Assess the morphology of the red blood cells.
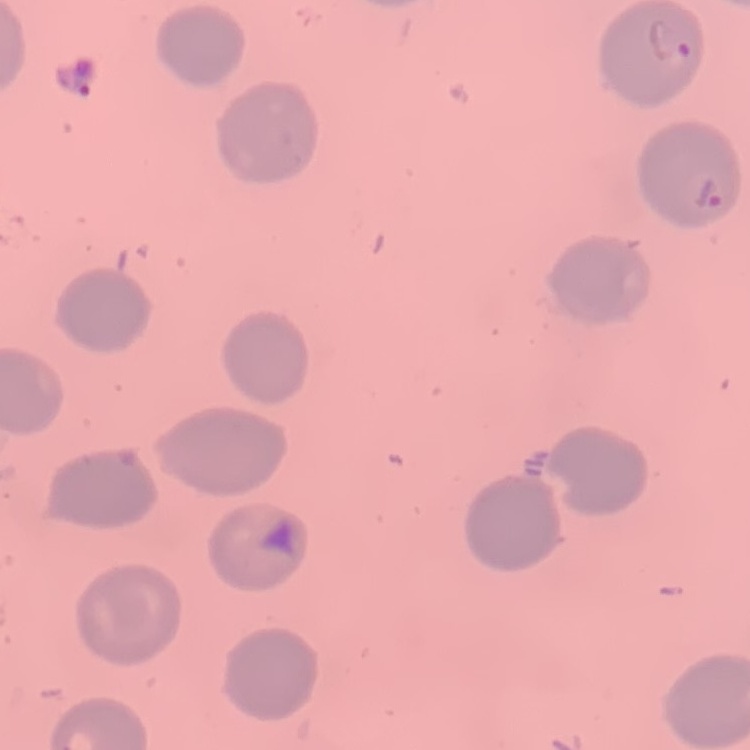
No rouleaux formation.

image type = one tile cut from a larger photomicrograph
stain = Field's or Giemsa
preparation = thin blood film